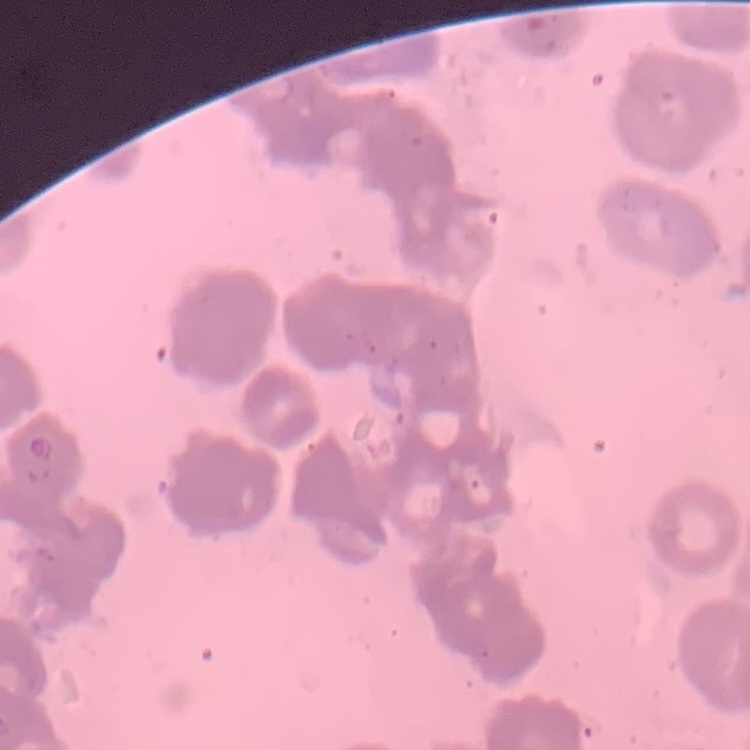
Summary:
  - Erythrocyte morphology: rouleaux formation
  - Stain: Field's or Giemsa
  - Image type: one tile cut from a larger photomicrograph
  - Preparation: thin blood film